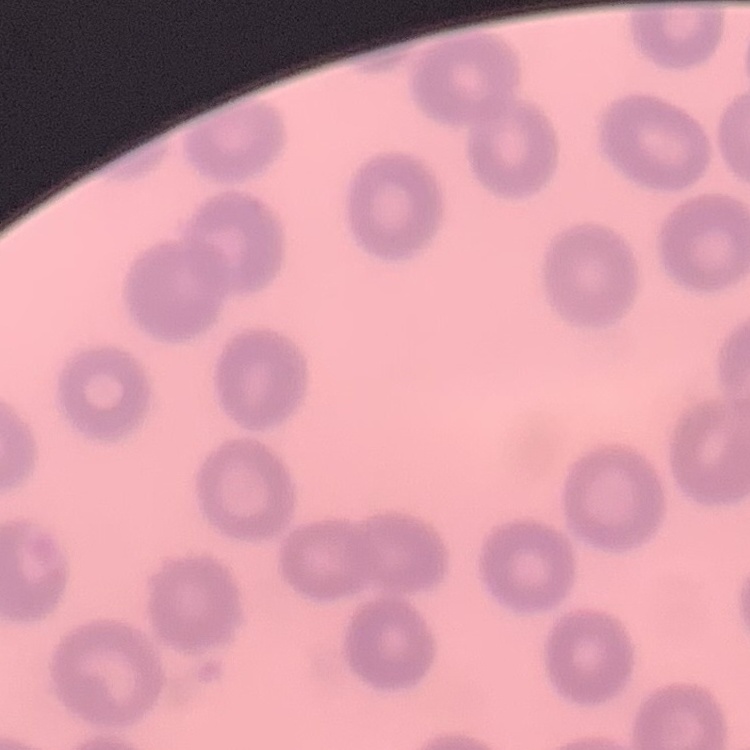
{
  "red_blood_cell_morphology": "no rouleaux formation",
  "preparation": "thin blood smear",
  "stain": "Field's or Giemsa",
  "image_type": "one tile cut from a larger photomicrograph"
}